Assess this cell for malaria.
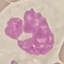

It is uninfected.

Summary:
  - Preparation: thin blood film
  - Capture: smartphone through the microscope eyepiece
  - Image type: automatically extracted cell patch, resized to 64 × 64 pixels
  - Stain: Giemsa